Point out every malaria parasite.
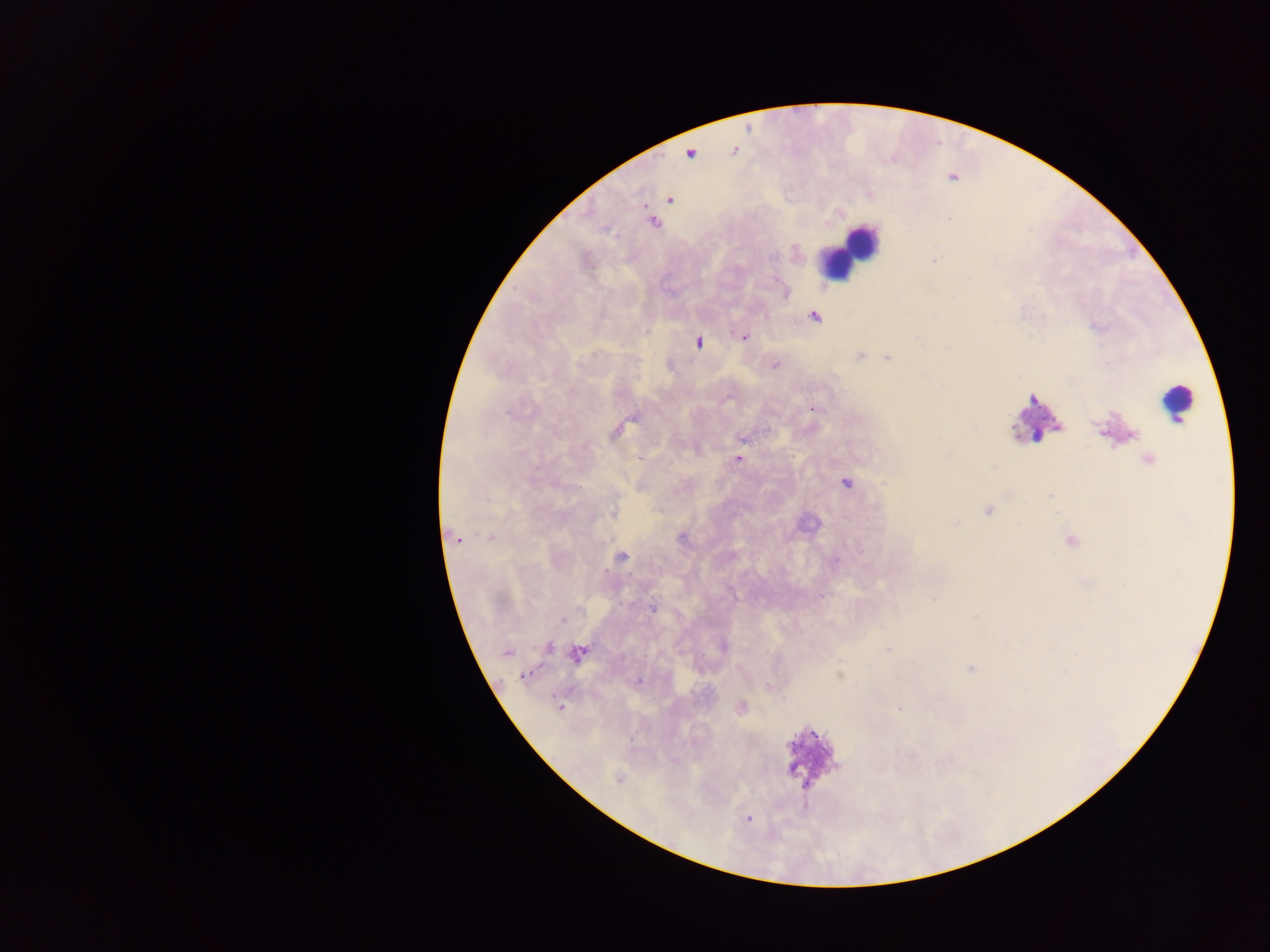

Approximate centers as {x, y} in pixels.
Malaria parasites: {734, 150}, {689, 154}, {669, 199}, {653, 222}, {784, 292}, {814, 316}, {743, 336}, {698, 341}, {860, 355}, {888, 357}, {775, 364}, {813, 407}, {632, 417}, {619, 429}, {742, 438}, {737, 458}, {1147, 459}, {845, 482}, {987, 510}, {614, 511}, {490, 536}, {454, 537}, {1071, 541}, {620, 557}, {931, 598}, {652, 608}, {562, 619}, {722, 646}, {547, 647}, {888, 648}, {506, 652}, {578, 653}, {971, 669}, {524, 674}, {637, 680}, {768, 686}, {559, 706}, {740, 708}, {900, 708}, {618, 779}, {748, 819}.

{
  "capture": "mobile-phone photograph through a microscope",
  "country": "Ghana",
  "preparation": "thick blood film",
  "field_of_view": "single",
  "image_size": "1270×952 pixels",
  "leukocyte_locations": "approximate centers as {x, y} in pixels: {849, 249}, {1178, 403}, {1032, 418}, {811, 759}"
}